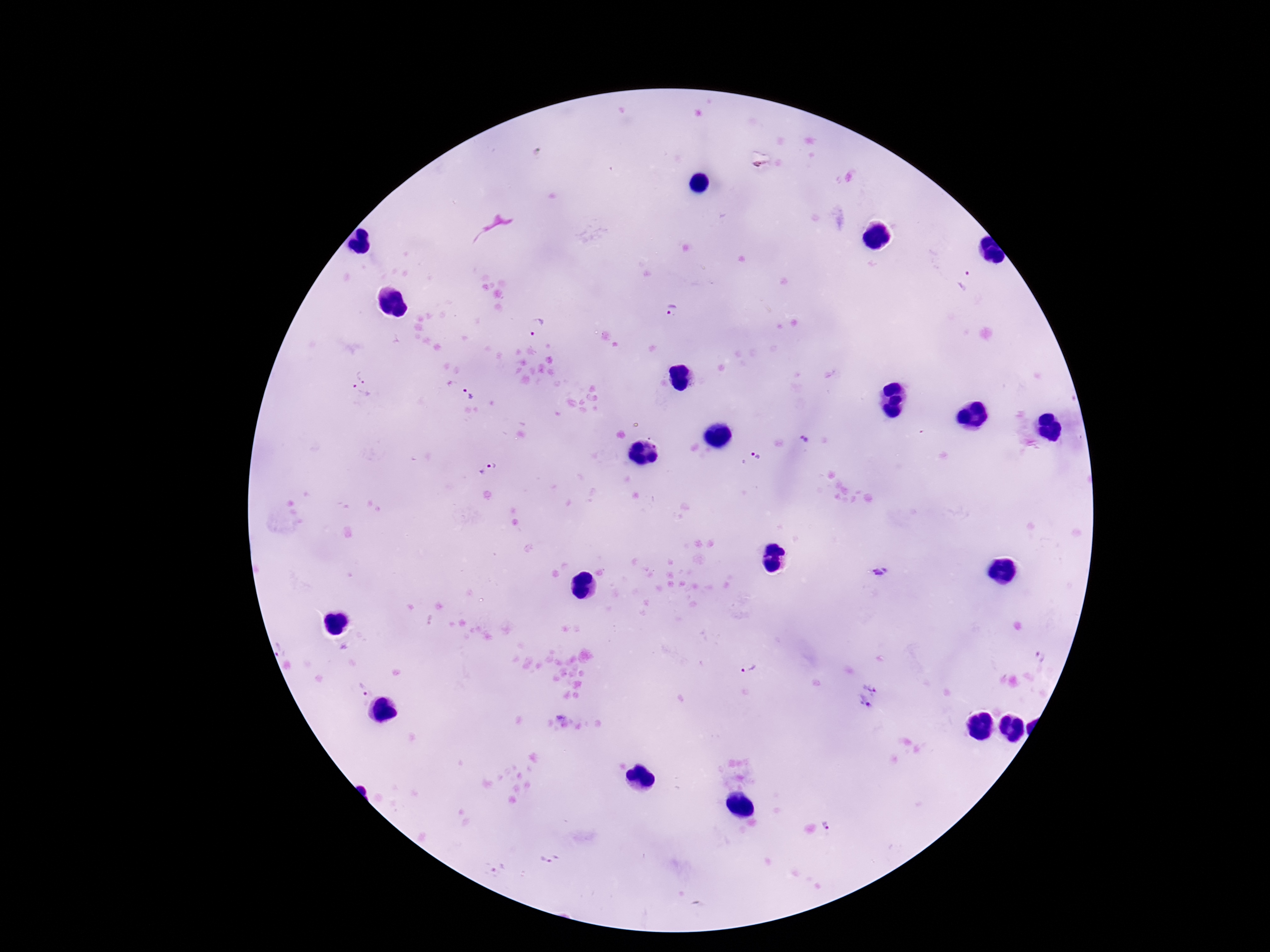

Approximate object centers, in pixels from the top-left corner. Plasmodium parasite locations: (x=969, y=283), (x=672, y=314), (x=539, y=327), (x=363, y=376), (x=359, y=396), (x=469, y=396), (x=803, y=439), (x=755, y=458), (x=488, y=469), (x=882, y=572), (x=1042, y=655), (x=750, y=668), (x=871, y=684), (x=360, y=688), (x=864, y=704), (x=562, y=720), (x=828, y=824), (x=549, y=859), (x=497, y=868). Giemsa-stained preparation. 100x magnification. Patient malaria status: infected. Image is 1270×952 pixels. Smartphone photograph taken through the microscope eyepiece. Thick blood smear. Single field of view.